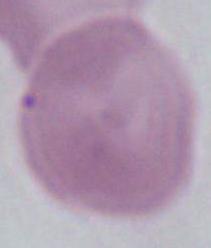

1000x magnification. Micrograph. A red blood cell is seen.